Report the malaria status of this cell.
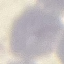
Uninfected.

stain = Giemsa
image type = automatically extracted cell patch, resized to 64 × 64 pixels
capture = smartphone camera at the microscope eyepiece
preparation = thin blood film